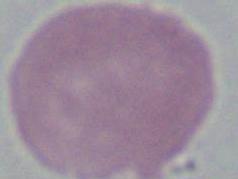
Summary:
  - Magnification: 1000x
  - Identification: red blood cell
  - Modality: micrograph